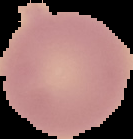

{
  "image_size": "133×139 pixels",
  "preparation": "thin blood film",
  "image_type": "segmented cell region on a black background",
  "result": "negative for Plasmodium parasites"
}